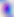
Photomicrograph. Toxoplasma gondii is shown. Captured at 400x magnification.